Assess the morphology of the red blood cells.
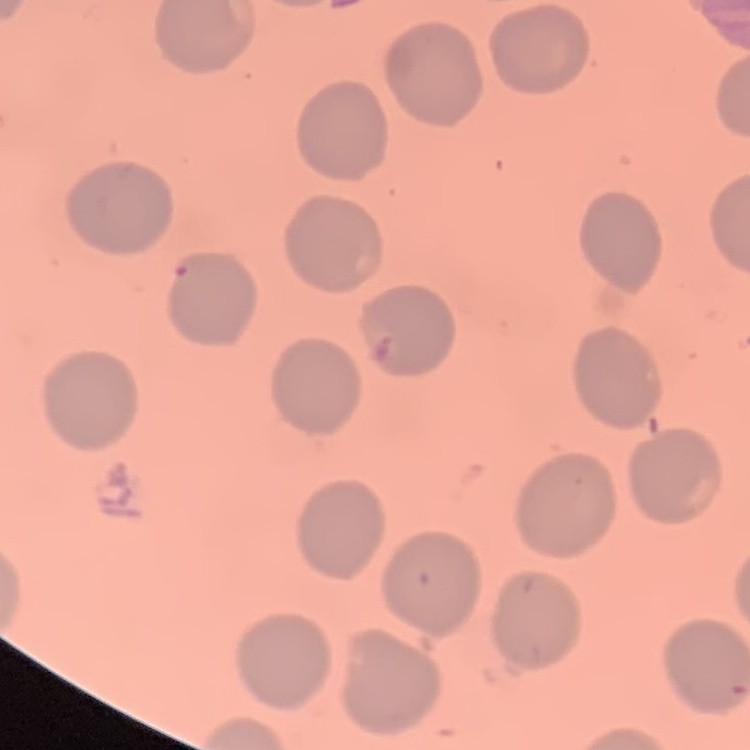

They show no rouleaux formation.

Thin peripheral smear. Square crop of a larger photomicrograph. Stained with either Field's or Giemsa.